Describe the morphology of the erythrocytes.
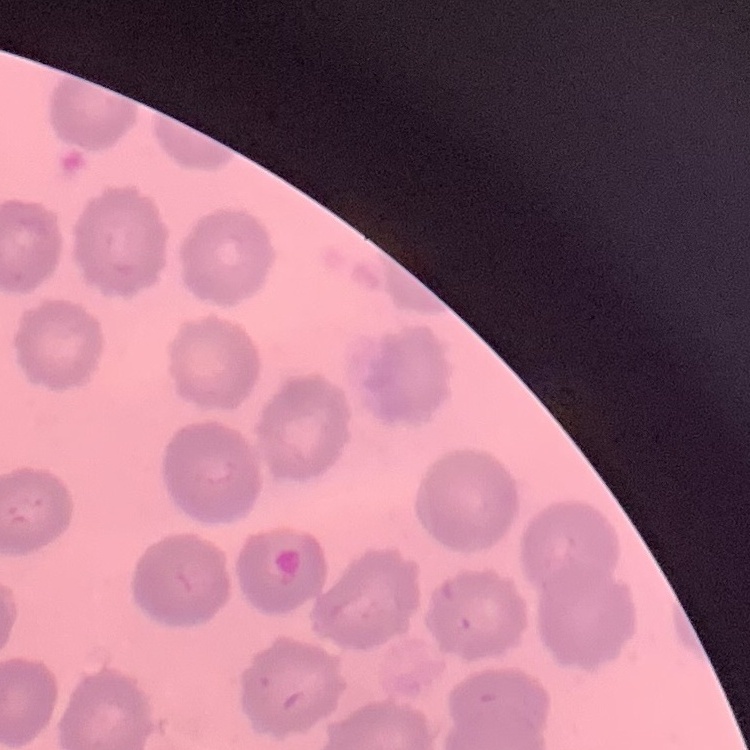
No rouleaux formation.

stain = Field's or Giemsa
image type = square crop of a larger photomicrograph
preparation = thin blood film